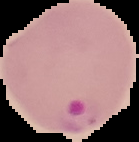
Summary:
  - Image size: 139×142 pixels
  - Preparation: thin blood film
  - Image type: segmented cell region on a black background
  - Malaria status: parasitized